Locate every Plasmodium parasite and every leukocyte.
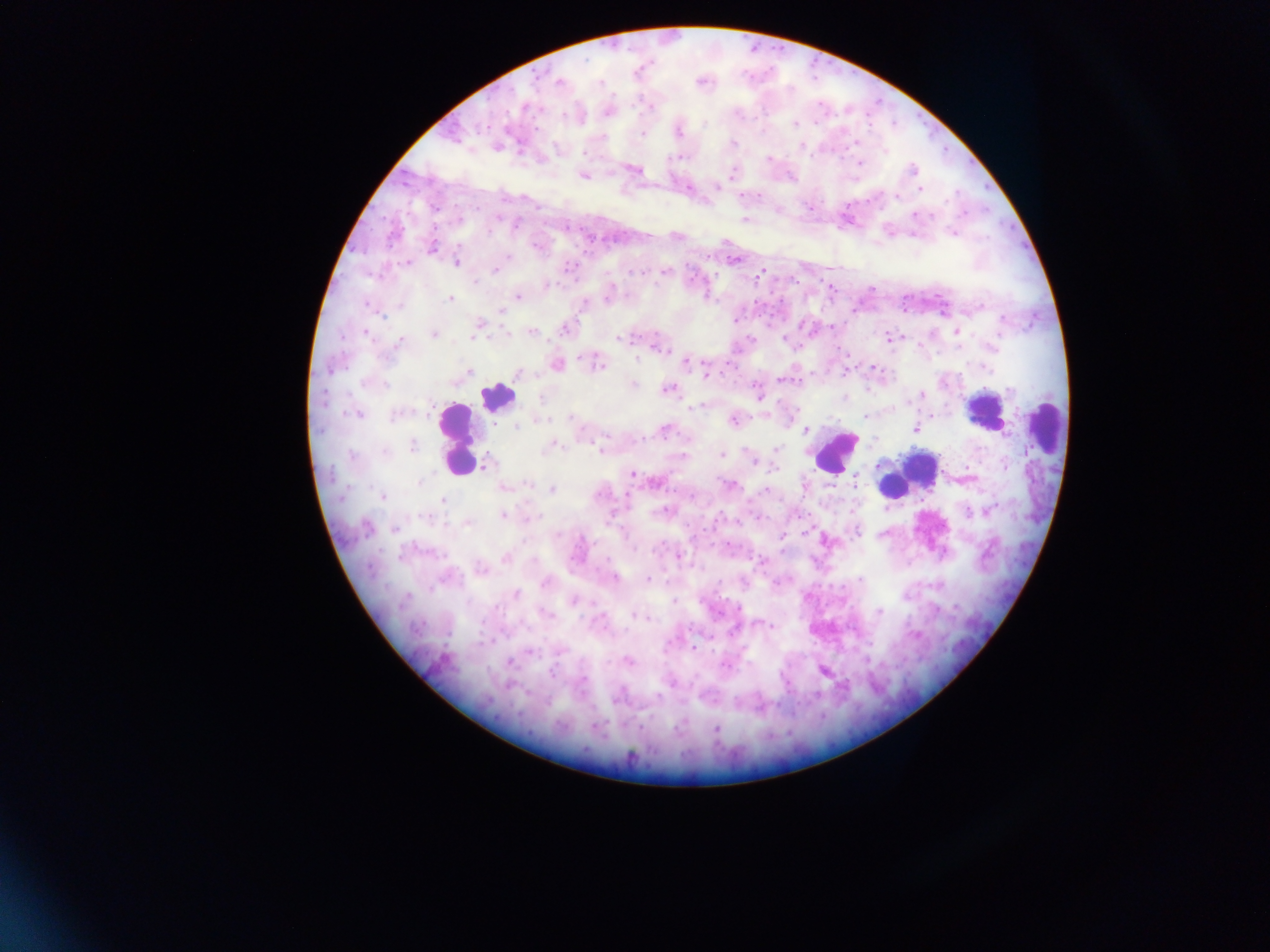

Approximate centers as (x, y) in pixels.
Plasmodium parasites: (559, 82), (599, 82), (651, 107), (525, 108), (564, 116), (816, 122), (704, 123), (795, 124), (679, 132), (642, 134), (603, 137), (855, 142), (733, 143), (801, 146), (885, 152), (584, 153), (677, 158), (769, 159), (861, 163), (633, 169), (913, 169), (732, 173), (583, 176), (717, 187), (920, 189), (757, 196), (897, 196), (434, 207), (809, 208), (779, 210), (915, 215), (744, 220), (516, 225), (489, 232), (952, 232), (536, 246), (432, 247), (507, 256), (734, 261), (455, 262), (407, 263), (495, 271), (664, 271), (635, 272), (759, 275), (475, 282), (547, 285), (871, 288), (518, 296), (450, 299), (607, 299), (585, 303), (368, 305), (501, 310), (382, 316), (1004, 319), (478, 325), (832, 326), (564, 328), (956, 331), (366, 333), (531, 333), (434, 334), (473, 337), (889, 337), (783, 338), (619, 339), (399, 341), (995, 345), (659, 347), (581, 358), (637, 358), (686, 363), (557, 365), (599, 365), (873, 368), (986, 368), (331, 369), (470, 372), (845, 372), (517, 374), (707, 375), (782, 380), (633, 384), (385, 385), (668, 390), (1008, 390), (756, 392), (922, 394), (845, 397), (541, 399), (698, 407), (356, 414), (397, 415), (765, 415), (865, 416), (570, 418), (540, 420), (733, 421), (517, 427), (915, 429), (806, 430), (664, 431), (413, 446), (551, 446), (776, 449), (600, 450), (385, 451), (722, 455), (353, 456), (684, 456), (753, 461), (486, 464), (879, 465), (775, 469), (632, 474), (419, 482), (855, 482), (527, 484), (729, 485), (504, 488), (551, 490), (765, 490), (382, 497), (442, 501), (664, 510), (968, 512), (504, 515), (537, 516), (424, 518), (467, 523), (366, 528), (395, 529), (857, 531), (883, 534), (782, 535), (634, 548), (678, 556), (506, 557), (480, 569), (614, 578), (648, 579), (860, 579), (546, 583), (516, 594), (406, 597), (573, 601), (674, 601), (879, 611), (547, 614), (634, 617), (645, 618), (759, 624), (772, 626), (667, 646), (694, 648), (530, 652), (628, 661), (509, 663), (725, 666), (823, 671), (553, 673), (672, 681), (658, 696), (716, 729).
Leukocytes: (497, 396), (984, 414), (1044, 424), (457, 440), (834, 452), (922, 467), (891, 486).

country = Ghana
preparation = thick blood film
capture = mobile-phone photograph through a microscope
image size = 1270×952 pixels
field of view = single